Report the malaria status.
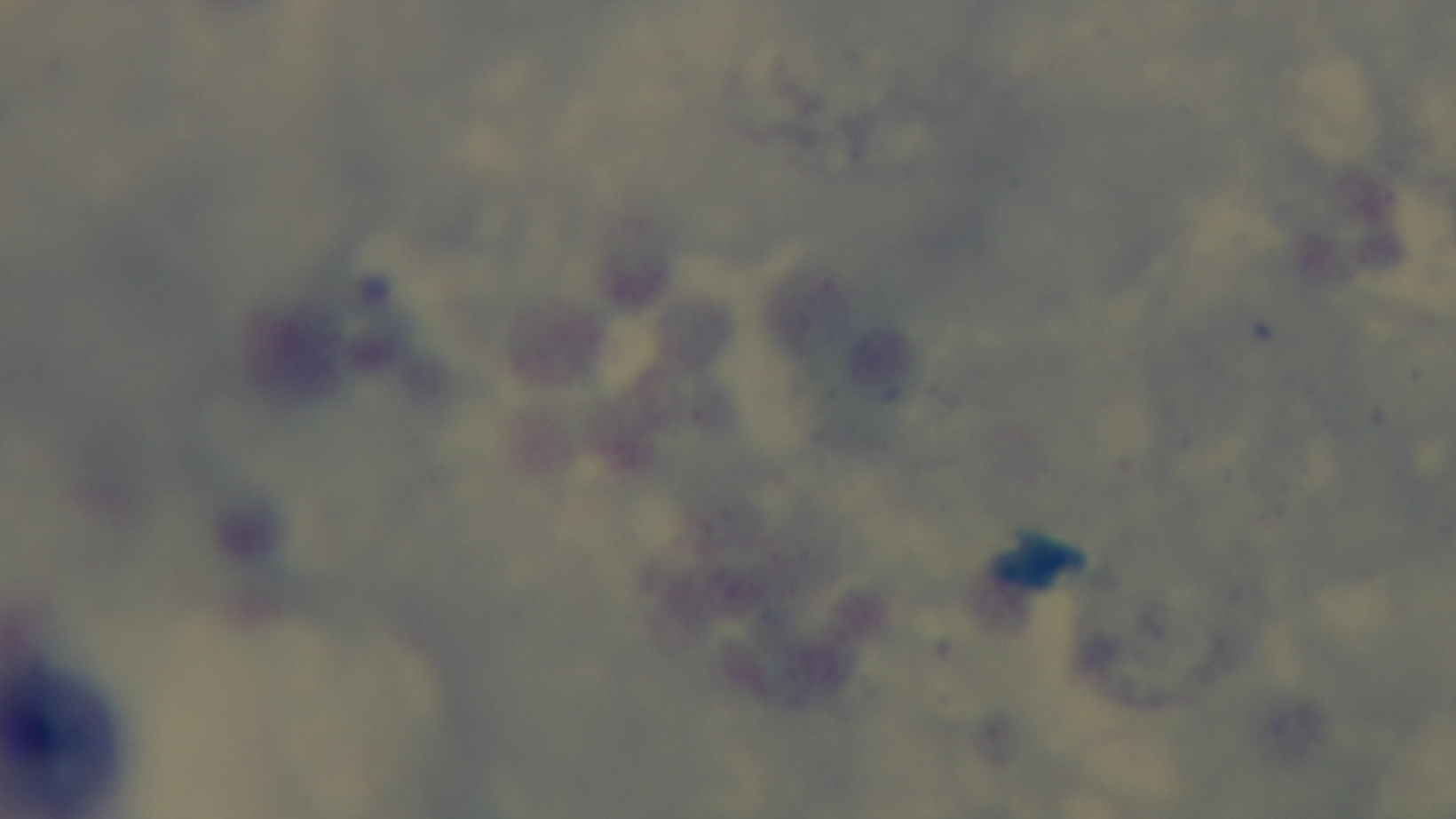

Uninfected.

{
  "capture": "mounted 4K digital camera",
  "stain": "Giemsa",
  "preparation": "thick blood film",
  "modality": "light microscopy",
  "objective": "100x oil immersion",
  "field_of_view": "single"
}